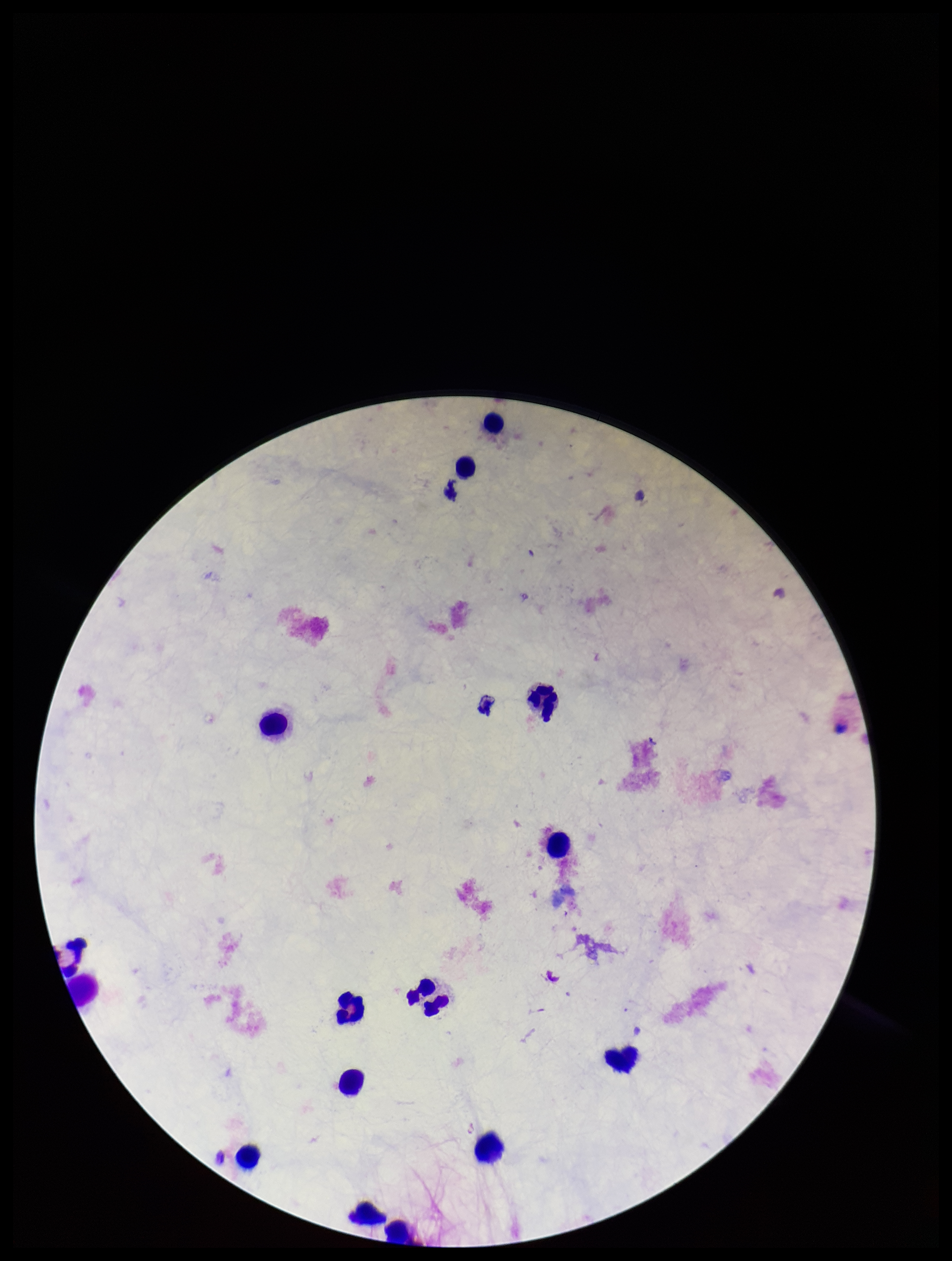

{
  "preparation": "thick blood smear",
  "patient_malaria_status": "negative",
  "parasite_count": 0,
  "plasmodium_parasites": "none seen",
  "capture": "smartphone photograph through the microscope eyepiece",
  "stain": "Giemsa",
  "field_of_view": "one from this slide",
  "leukocyte_count": 14,
  "image_size": "952×1261 pixels"
}